Name the cell type shown.
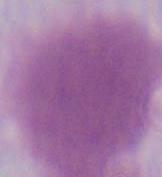

This is an erythrocyte.

Summary:
  - Modality: micrograph
  - Magnification: 1000x